Locate and identify every blood parasite.
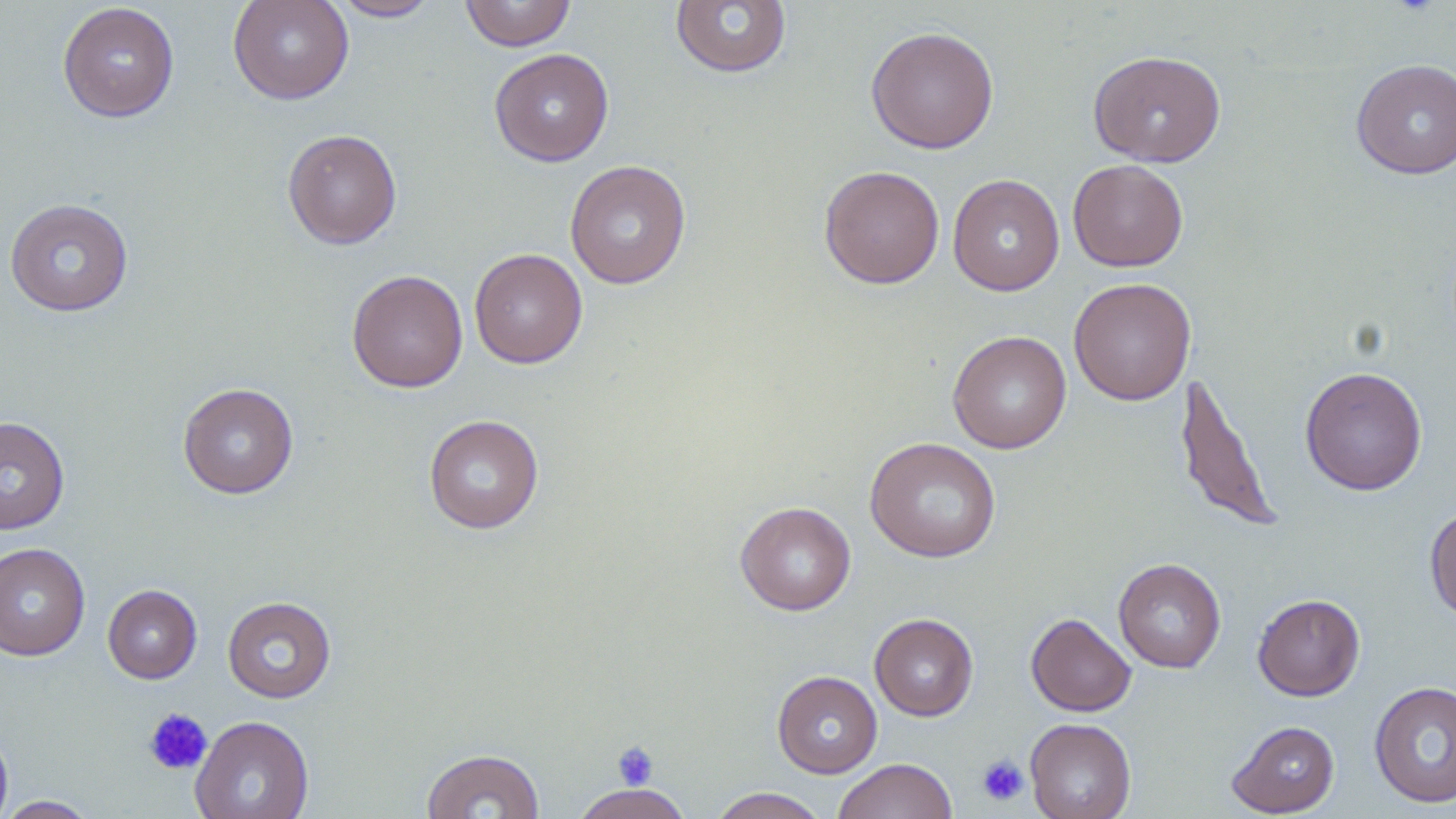
No blood parasites seen.

slide_level_diagnosis: negative for blood parasites
preparation: thin blood film
modality: light microscopy
magnification: 1000x
image_size: 1456×819 pixels
platelet_locations: 'approximate bounding boxes as named x1/y1/x2/y2 corners in pixels: (x1=142, y1=707, x2=212, y2=775), (x1=612, y1=740, x2=660, y2=790), (x1=976, y1=754, x2=1030, y2=806)'
field_of_view: single
stain: May-Grünwald-Giemsa
uninfected_red_blood_cell_locations: 'approximate bounding boxes as named x1/y1/x2/y2 corners in pixels: (x1=228, y1=0, x2=354, y2=104), (x1=330, y1=0, x2=442, y2=21), (x1=459, y1=0, x2=576, y2=51), (x1=670, y1=1, x2=792, y2=78), (x1=57, y1=2, x2=180, y2=122), (x1=865, y1=25, x2=1000, y2=154), (x1=489, y1=48, x2=614, y2=166), (x1=1087, y1=49, x2=1226, y2=167), (x1=1351, y1=59, x2=1456, y2=179), (x1=283, y1=129, x2=403, y2=249), (x1=1068, y1=159, x2=1188, y2=272), (x1=564, y1=160, x2=691, y2=289), (x1=819, y1=165, x2=945, y2=289), (x1=948, y1=174, x2=1065, y2=296), (x1=4, y1=198, x2=134, y2=316), (x1=469, y1=248, x2=588, y2=368), (x1=347, y1=269, x2=468, y2=393), (x1=1069, y1=277, x2=1196, y2=405), (x1=947, y1=330, x2=1071, y2=454), (x1=1300, y1=366, x2=1427, y2=496), (x1=1173, y1=369, x2=1282, y2=533), (x1=178, y1=382, x2=299, y2=499), (x1=423, y1=414, x2=544, y2=533), (x1=0, y1=415, x2=70, y2=535), (x1=864, y1=436, x2=1002, y2=562), (x1=735, y1=501, x2=856, y2=615), (x1=1424, y1=504, x2=1456, y2=622), (x1=0, y1=542, x2=91, y2=661), (x1=1113, y1=558, x2=1226, y2=673), (x1=103, y1=584, x2=202, y2=683), (x1=1252, y1=593, x2=1365, y2=701), (x1=223, y1=596, x2=336, y2=702), (x1=1026, y1=612, x2=1136, y2=716), (x1=870, y1=614, x2=978, y2=721), (x1=772, y1=670, x2=882, y2=778), (x1=1369, y1=680, x2=1456, y2=808), (x1=190, y1=715, x2=314, y2=819), (x1=1025, y1=717, x2=1136, y2=819), (x1=1226, y1=720, x2=1340, y2=817), (x1=0, y1=721, x2=13, y2=819), (x1=421, y1=748, x2=545, y2=819), (x1=832, y1=758, x2=959, y2=819), (x1=568, y1=782, x2=694, y2=819), (x1=708, y1=787, x2=829, y2=819), (x1=0, y1=796, x2=102, y2=818)'